State which cell type is depicted.
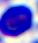
A leukocyte.

modality = micrograph
magnification = 400x